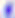

Photomicrograph. Captured at 400x magnification. Toxoplasma gondii is seen.